Point out each Plasmodium parasite.
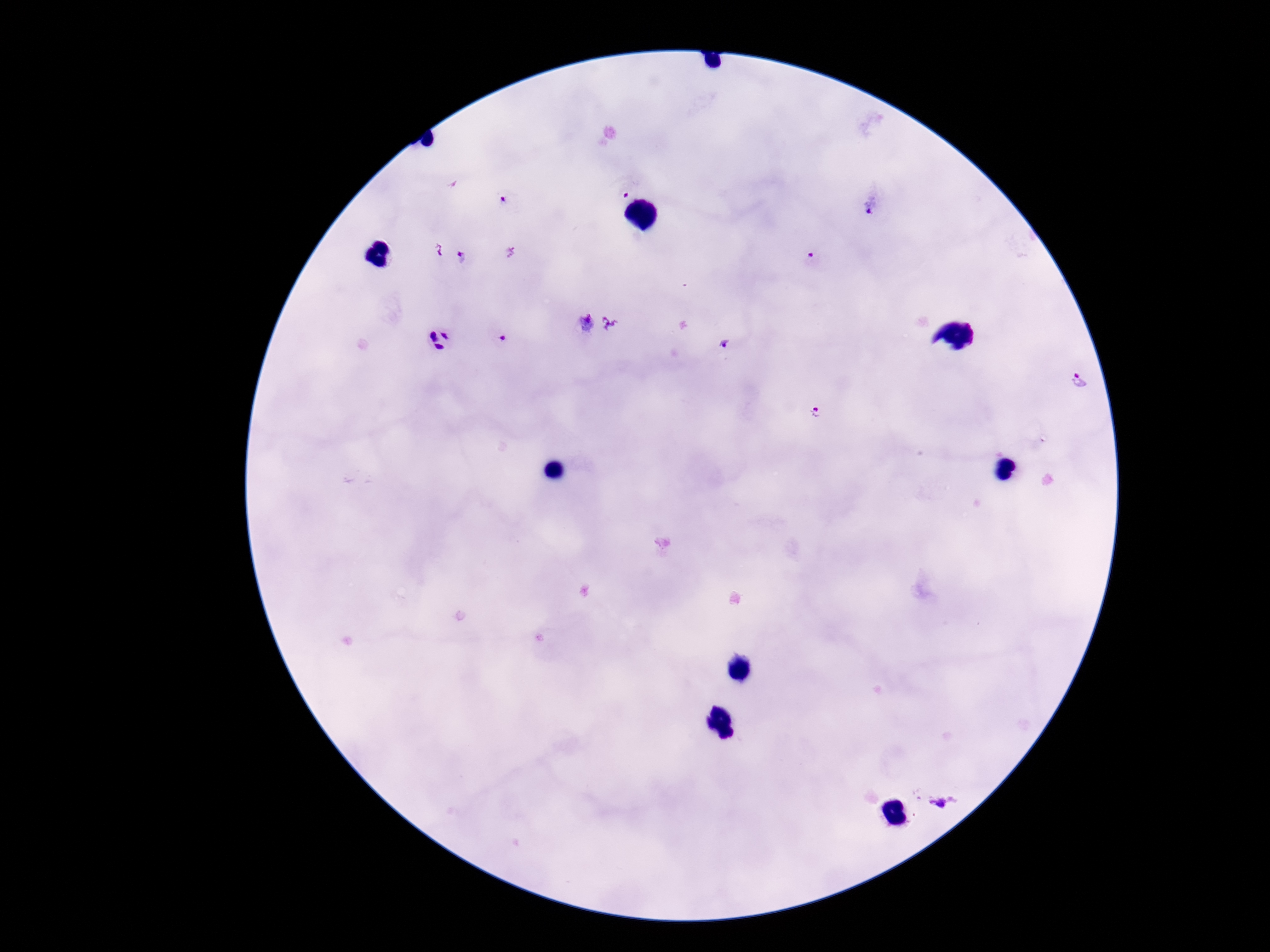

Approximate centers as (x, y) in pixels.
Plasmodium parasites: (626, 190), (504, 203), (871, 206), (462, 258), (812, 261), (586, 323), (610, 323), (497, 334), (439, 340), (724, 343), (1078, 379), (815, 412), (941, 802).

field of view = single
patient malaria status = positive
magnification = 100x
image size = 1270×952 pixels
stain = Giemsa
preparation = thick peripheral-blood smear
capture = smartphone camera through the microscope eyepiece